Outline every parasitised red blood cell, every trophozoite, every gametocyte, every leukocyte, and every artifact (platelet-like body, stain precipitate, or debris).
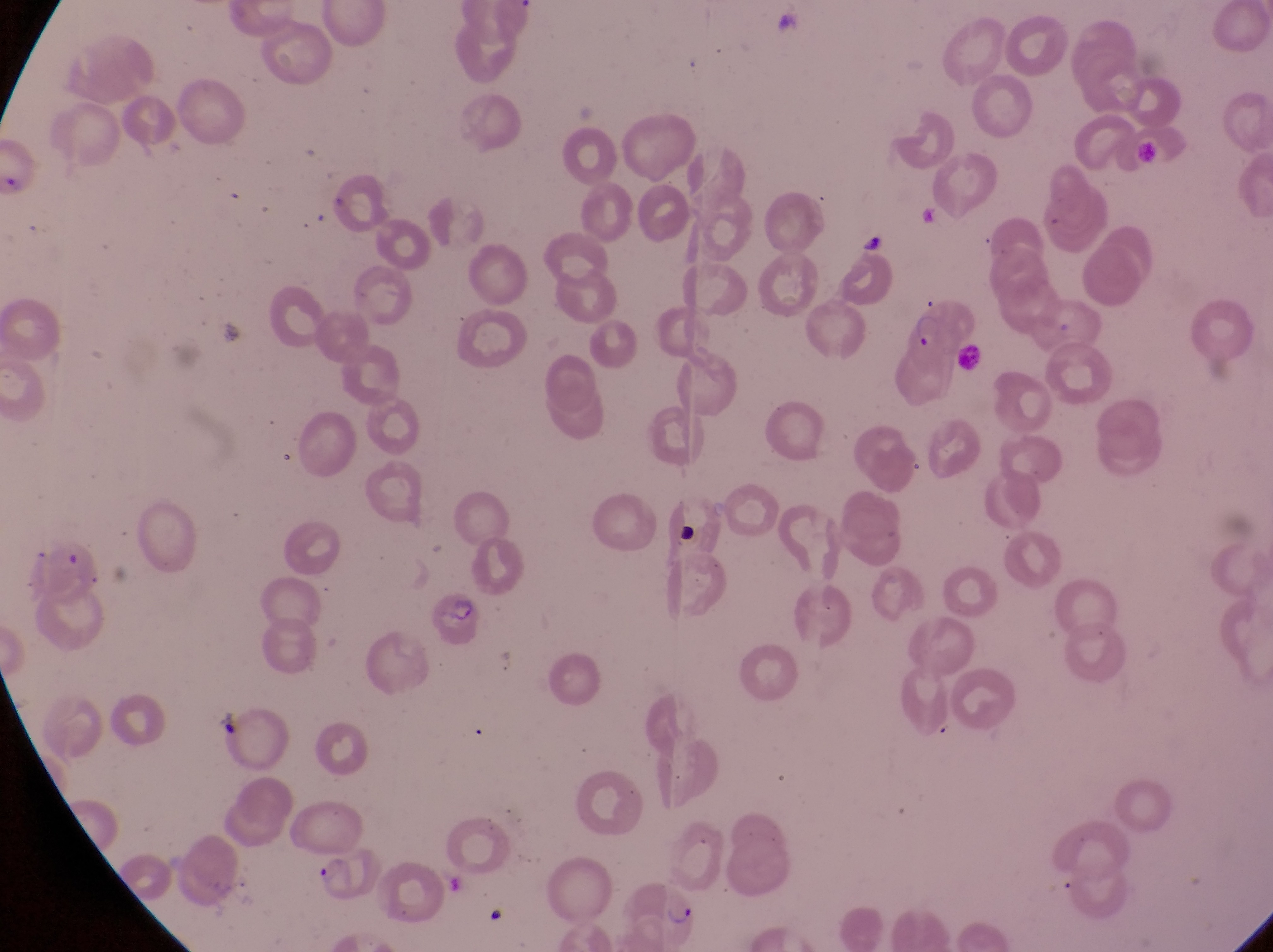

Approximate bounding boxes as [left, top, right, bottom] in pixels.
Parasitised red blood cells: [909, 305, 948, 350], [630, 882, 699, 937].
Trophozoites: [312, 847, 352, 882].
No leukocytes observed.

Summary:
  - Country: Uganda
  - Preparation: thin blood film
  - Image size: 1273×952 pixels
  - Field of view: single
  - Magnification: 1000x
  - Capture: smartphone photograph through the eyepiece of an Olympus CX-23 microscope